Locate every Plasmodium parasite.
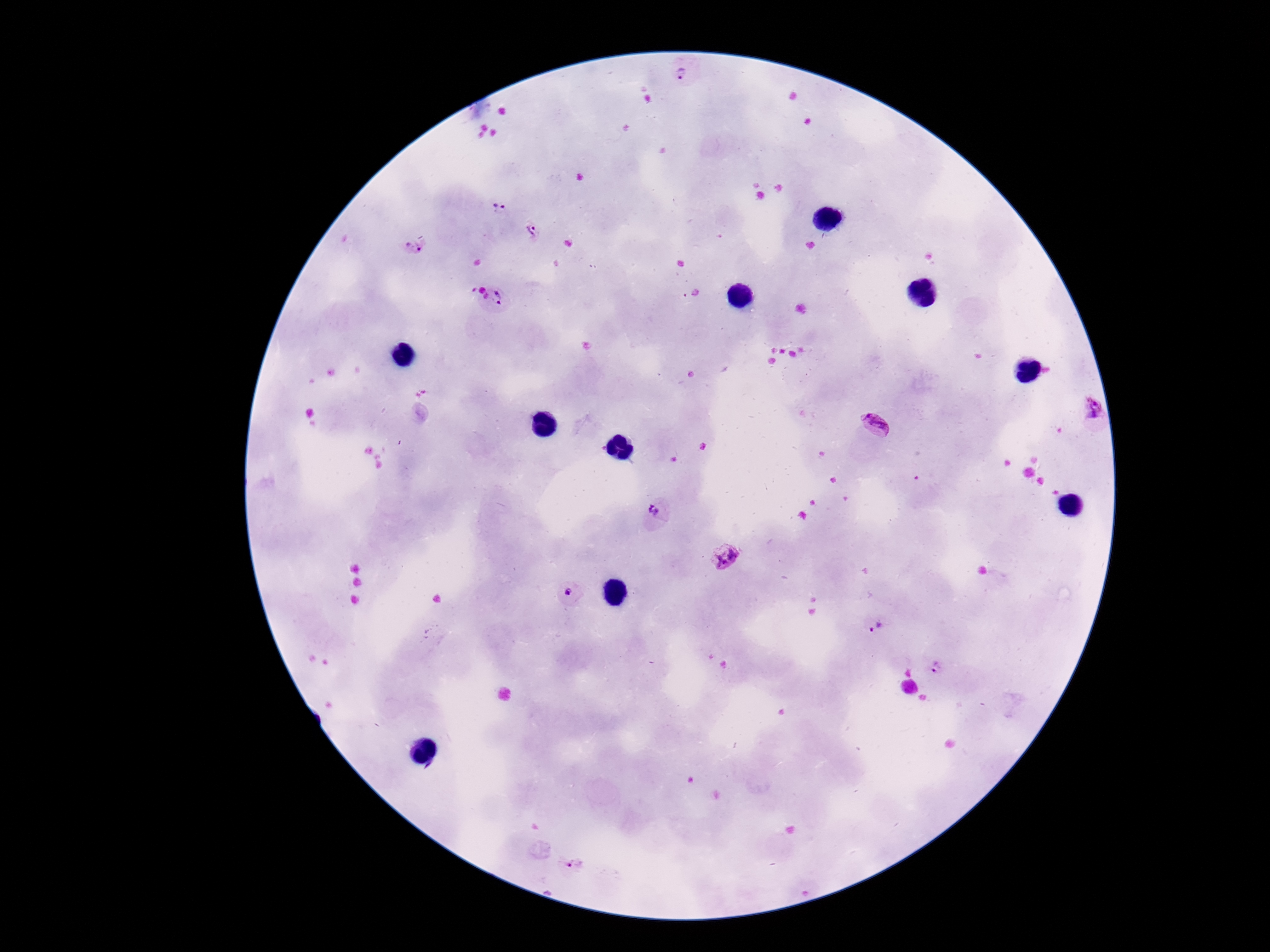
Approximate centers as (x, y) in pixels.
Plasmodium parasites: (683, 68), (499, 208), (533, 228), (413, 247), (504, 299), (1084, 411), (876, 424), (658, 510), (726, 556), (568, 593), (874, 627), (939, 666), (573, 864).

Summary:
  - Field of view: single
  - Capture: smartphone camera through the microscope eyepiece
  - Stain: Giemsa
  - Magnification: 100x
  - Patient malaria status: infected
  - Image size: 1270×952 pixels
  - Preparation: thick blood smear